Identify the parasite.
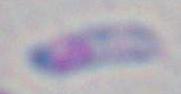
This is Toxoplasma gondii.

Summary:
  - Modality: micrograph
  - Magnification: 1000x